Give the position of every malaria parasite.
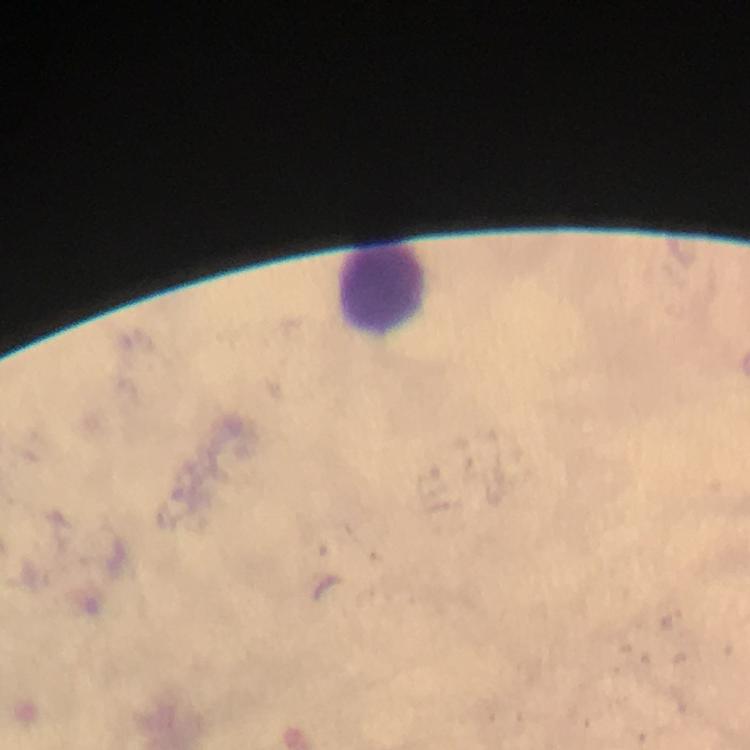

No malaria parasites seen.

Approximate object centers, in pixels from the top-left corner.
Summary:
  - Leukocyte locations: (x=383, y=288)
  - Stain: Giemsa
  - Preparation: thick smear
  - Context: from a malaria diagnostic workup
  - Immersion oil: used
  - Cropped from: a single field of view
  - Image size: 750×750 pixels
  - Capture: smartphone photograph through a microscope
  - Magnification: 100x